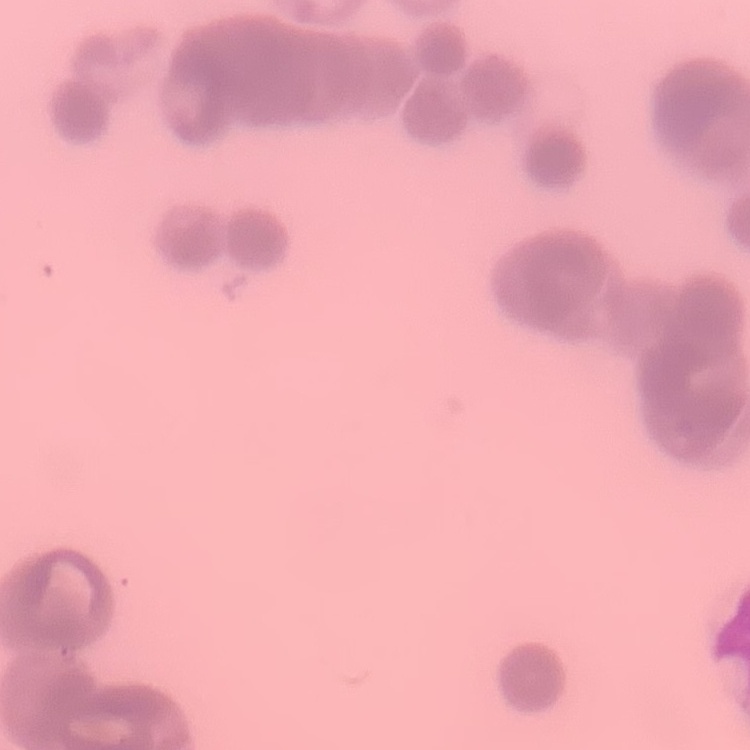 The erythrocytes show rouleaux formation. Thin blood smear. One tile cut from a larger photomicrograph. Field's or Giemsa stain.